Classify this cell by malaria status.
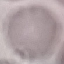

It is uninfected.

stain = Giemsa
image type = cell patch, automatically extracted from a larger field of view and resized to 64 × 64 pixels
capture = smartphone camera at the microscope eyepiece
preparation = thin smear